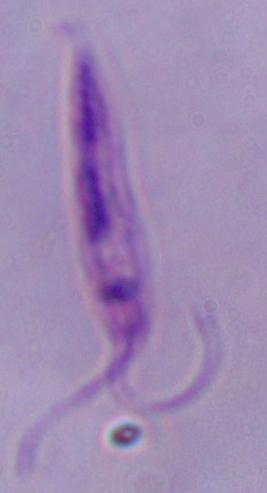 Photomicrograph. Captured at 1000x magnification. A Leishmania parasite is shown.